Identify the parasite.
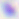
Toxoplasma gondii.

Summary:
  - Magnification: 400x
  - Modality: photomicrograph